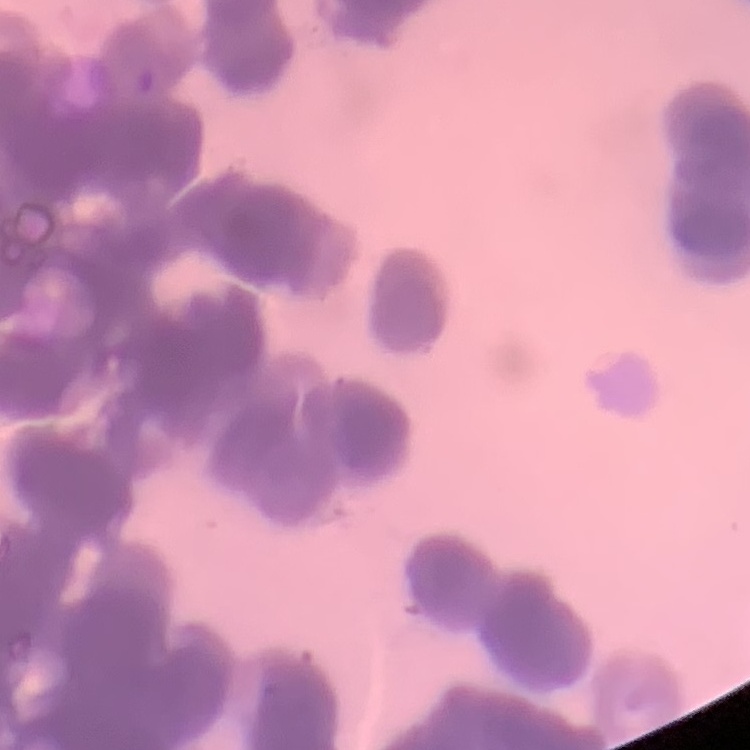
The erythrocytes exhibit rouleaux formation. One tile cut from a larger photomicrograph. Field's or Giemsa stain. Thin blood smear.